Locate and identify every blood parasite.
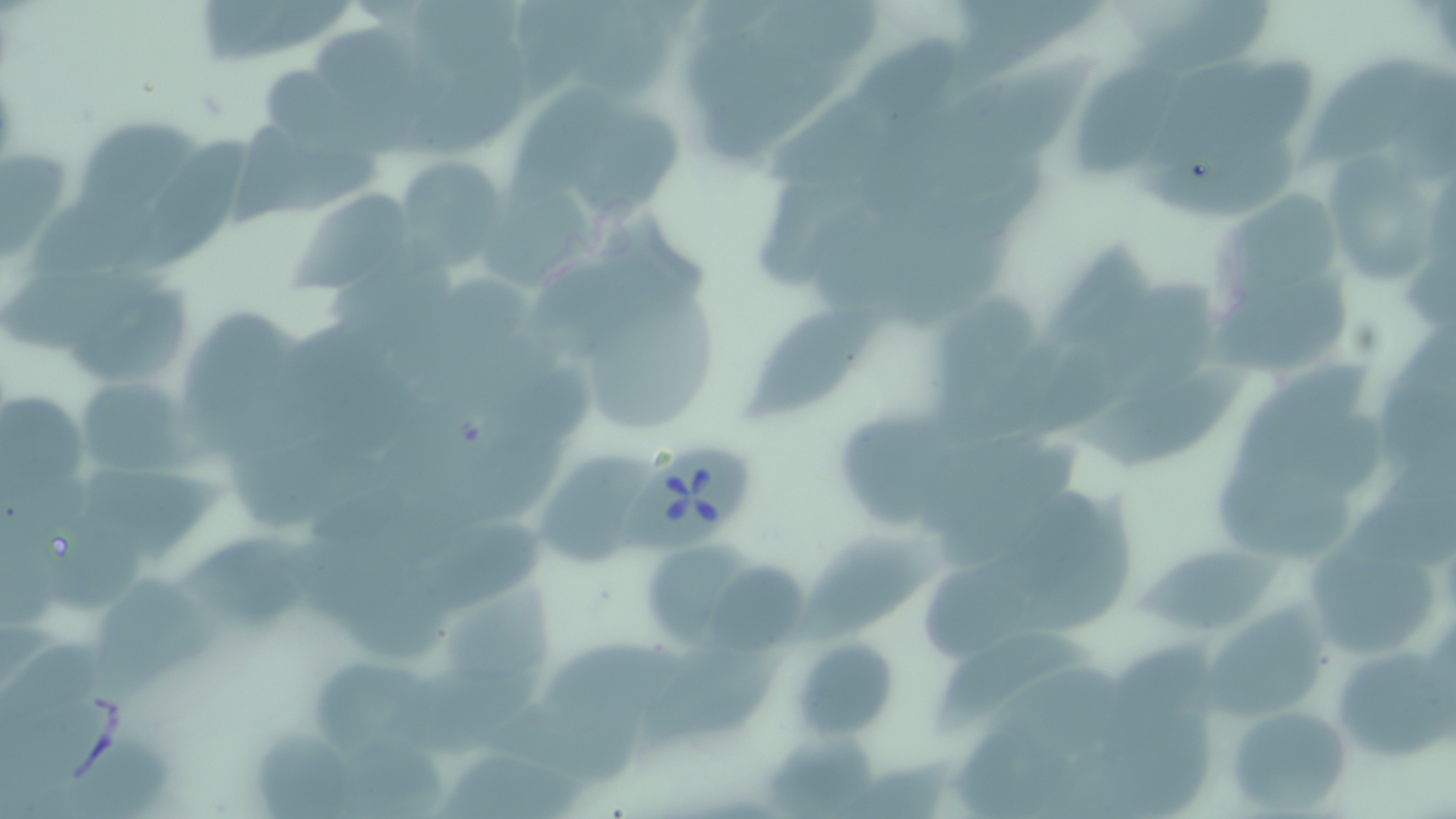
Approximate bounding boxes as [x1, y1, x2, y2] in pixels.
Babesia divergens-infected red blood cells: [620, 441, 762, 554].
No Plasmodium falciparum, Plasmodium ovale, Plasmodium malariae, Plasmodium vivax, or Trypanosoma brucei observed.

slide-level diagnosis = Babesia divergens
stain = May-Grünwald-Giemsa
modality = light microscopy
field of view = one of a larger specimen
image size = 1456×819 pixels
magnification = 1000x
preparation = thin blood smear
uninfected red blood cell locations = approximate bounding boxes as [x1, y1, x2, y2] in pixels: [191, 0, 340, 71], [511, 0, 611, 94], [760, 5, 881, 77], [417, 6, 543, 68], [845, 37, 967, 160], [394, 46, 541, 167], [1074, 49, 1190, 179], [955, 53, 1103, 166], [1204, 53, 1317, 164], [1308, 53, 1446, 170], [258, 64, 348, 145], [767, 93, 874, 188], [570, 103, 684, 216], [81, 118, 203, 210], [240, 120, 382, 223], [138, 128, 256, 276], [1326, 152, 1435, 284], [393, 158, 508, 263], [483, 172, 602, 299], [31, 187, 169, 287], [296, 188, 413, 290], [1215, 190, 1343, 296], [803, 207, 926, 321], [1042, 247, 1173, 365], [323, 250, 449, 347], [3, 264, 142, 359], [1107, 267, 1232, 385], [1211, 270, 1361, 374], [422, 275, 531, 410], [69, 280, 193, 377], [584, 295, 718, 428], [929, 297, 1044, 411], [740, 300, 889, 424], [181, 305, 299, 443], [1381, 310, 1456, 469], [1236, 349, 1373, 477], [1069, 357, 1257, 477], [73, 377, 192, 478], [3, 384, 96, 505], [830, 399, 1024, 532], [237, 438, 403, 525], [539, 447, 657, 558], [1357, 456, 1456, 576], [92, 458, 225, 560], [1215, 465, 1366, 564], [984, 482, 1103, 608], [1032, 494, 1140, 632], [46, 497, 150, 608], [428, 511, 563, 607], [796, 530, 956, 652], [1139, 534, 1282, 636], [187, 535, 343, 633], [1310, 541, 1438, 656], [644, 545, 775, 655], [308, 560, 450, 670], [703, 564, 814, 658], [99, 570, 223, 697], [446, 585, 560, 683], [1206, 598, 1327, 730], [0, 627, 119, 769], [550, 627, 689, 725], [933, 628, 1087, 734], [792, 636, 899, 740], [631, 637, 796, 751], [1095, 639, 1235, 750], [1329, 643, 1452, 764], [306, 657, 436, 754], [1226, 703, 1355, 814], [955, 715, 1079, 819], [1081, 717, 1217, 819], [771, 729, 879, 819], [59, 733, 186, 819], [439, 744, 594, 819]